Describe the morphology of the erythrocytes.
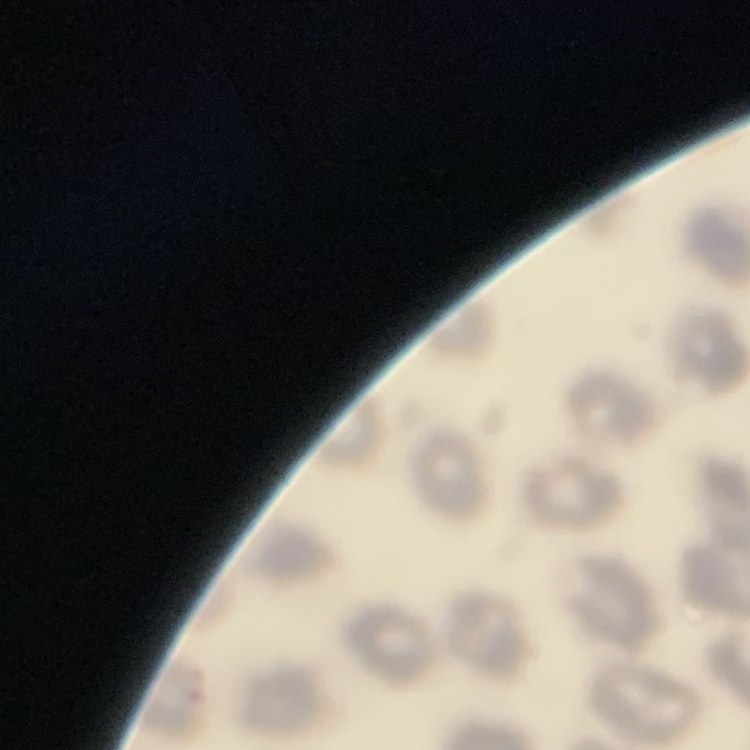
No rouleaux formation.

Field's or Giemsa stain. Thin blood film. Square crop of a larger photomicrograph.